Assess this cell for malaria.
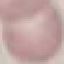

Uninfected.

Summary:
  - Capture: smartphone camera at the microscope eyepiece
  - Image type: automatically extracted cell patch, resized to 64 × 64 pixels
  - Stain: Giemsa
  - Preparation: thin smear